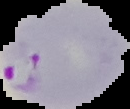
Malaria status: parasitized. From a thin blood smear. Cell region segmented out of the field of view; the surrounding area is masked to black. Image is 130×109 pixels.